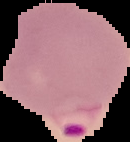
Summary:
  - Image type: cell region segmented out of the field of view; surrounding area masked to black
  - Result: malaria parasites identified
  - Preparation: thin blood smear
  - Image size: 130×142 pixels